Give the position of every Plasmodium parasite.
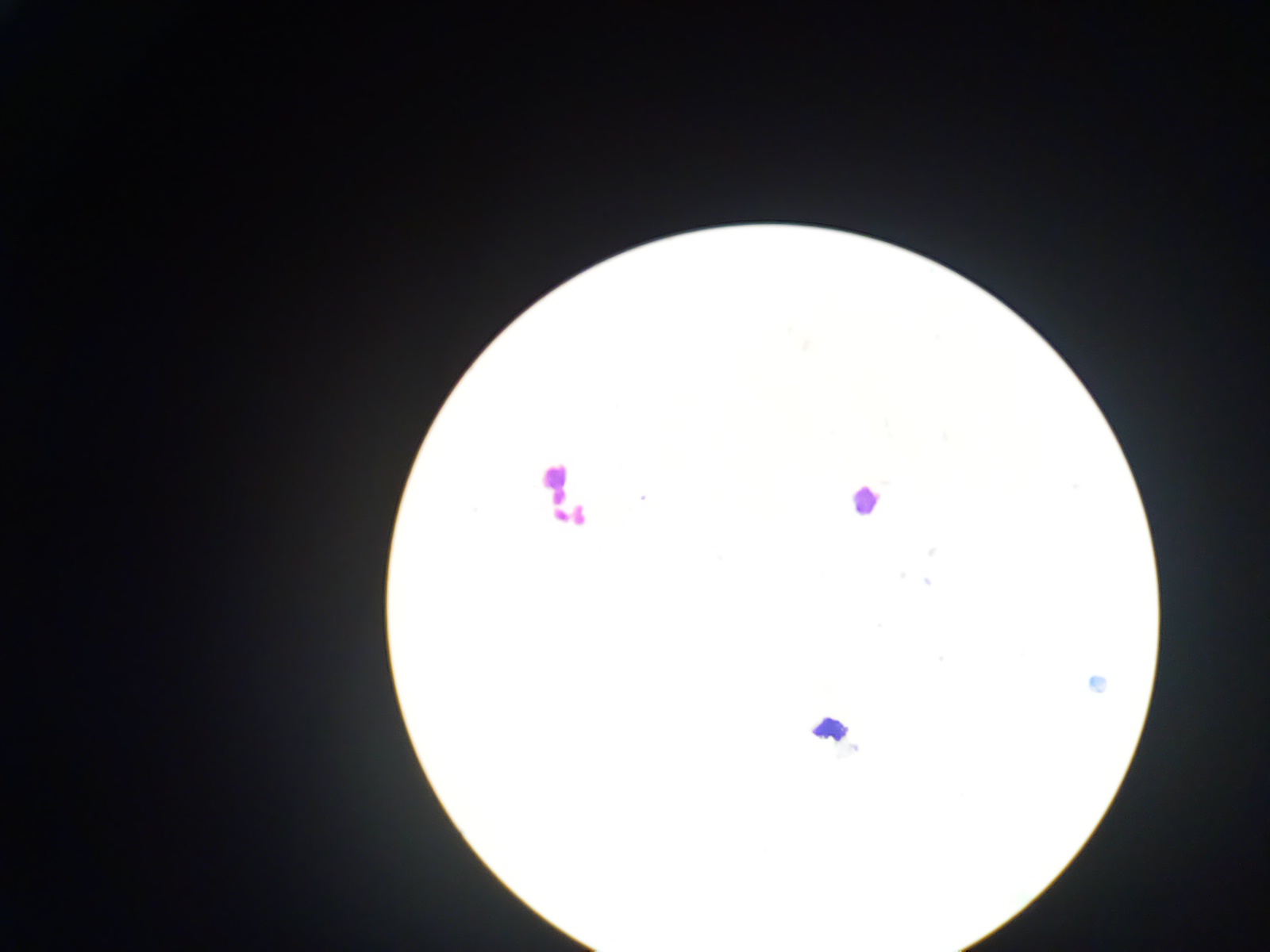
Approximate centers as [x, y] in pixels.
Plasmodium parasites: [642, 497], [474, 510], [932, 551], [720, 556], [901, 575], [916, 579], [927, 581], [879, 626], [939, 658], [1095, 682].

Summary:
  - Leukocyte locations: [553, 480], [864, 499], [569, 513], [829, 728]
  - Preparation: thick blood smear
  - Image size: 1270×952 pixels
  - Field of view: single
  - Capture: mobile-phone photograph through a microscope
  - Country: Ghana